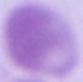

Summary:
  - Identification: erythrocyte
  - Magnification: 1000x
  - Modality: micrograph